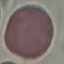

malaria status = uninfected
capture = smartphone camera at the microscope eyepiece
image type = cell patch, automatically extracted from a larger field of view and resized to 64 × 64 pixels
preparation = thin smear
stain = Giemsa